Assess this cell for malaria.
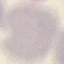
It is uninfected.

Thin blood film. Acquired by smartphone through the microscope eyepiece. Giemsa-stained preparation. Automatically extracted cell patch, resized to 64 × 64 pixels.